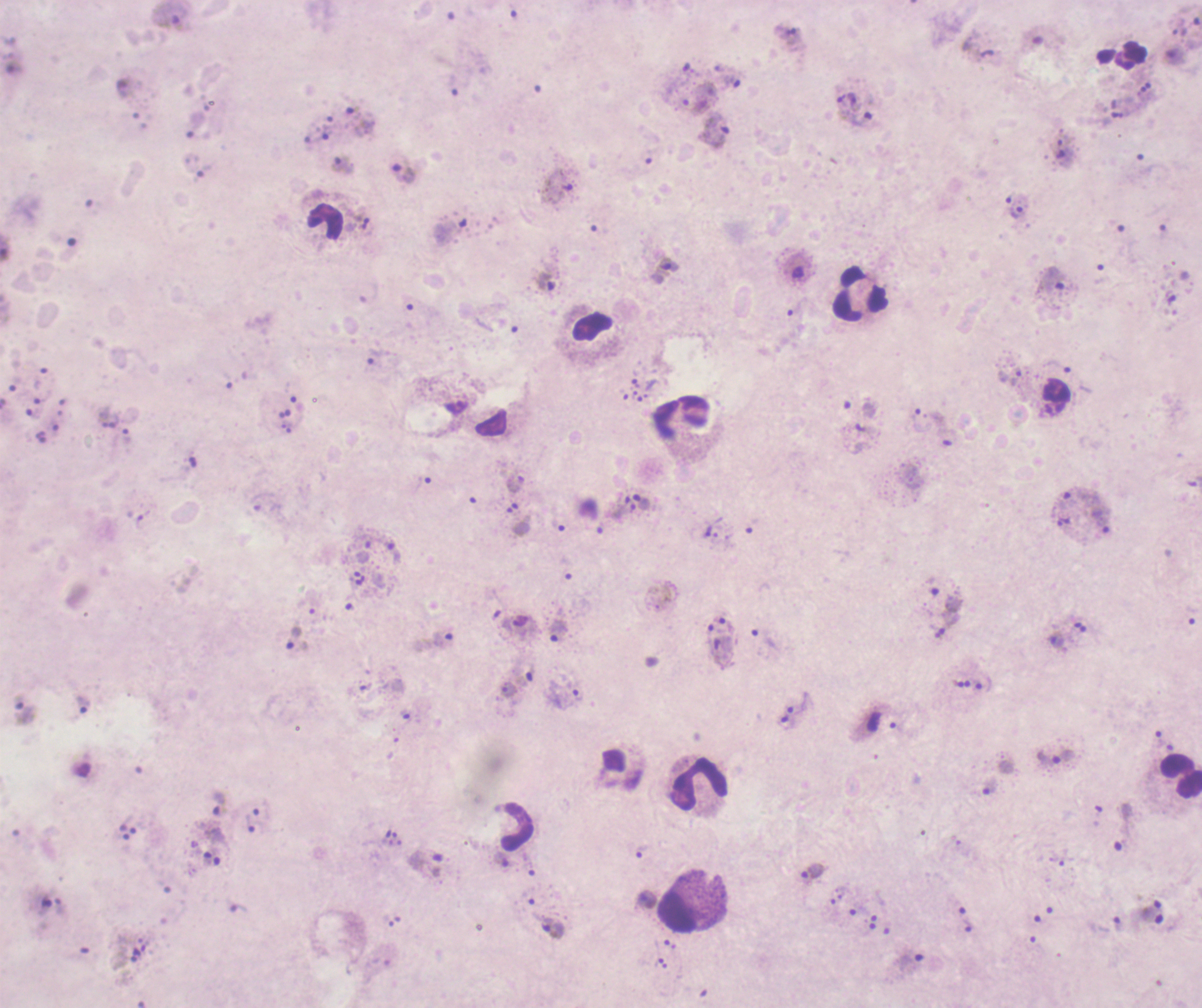
Approximate object centers, in pixels from the top-left corner. Trophozoite locations: (x=792, y=38), (x=856, y=117), (x=360, y=122), (x=714, y=128), (x=343, y=165), (x=403, y=174), (x=669, y=264), (x=546, y=282), (x=643, y=502), (x=711, y=531), (x=557, y=632), (x=1056, y=640), (x=507, y=689), (x=82, y=705), (x=1056, y=757), (x=219, y=803), (x=643, y=852), (x=427, y=863), (x=812, y=871), (x=1118, y=924), (x=552, y=928). Leukocyte locations: (x=325, y=222), (x=859, y=292), (x=682, y=416), (x=1181, y=777), (x=700, y=785), (x=517, y=827), (x=681, y=914). 100x magnification. Background quality: poor. Thick blood film. Result: malaria parasites identified. Image is 1202×1008 pixels. Previously used in an actual diagnosis. Coloration quality: bad. One field from this slide. Romanowsky-stained preparation.